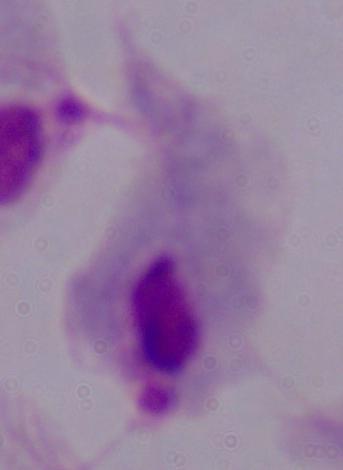
Summary:
  - Magnification: 1000x
  - Modality: photomicrograph
  - Identification: trichomonad